Give the extent of all Plasmodium ovale-infected red blood cells.
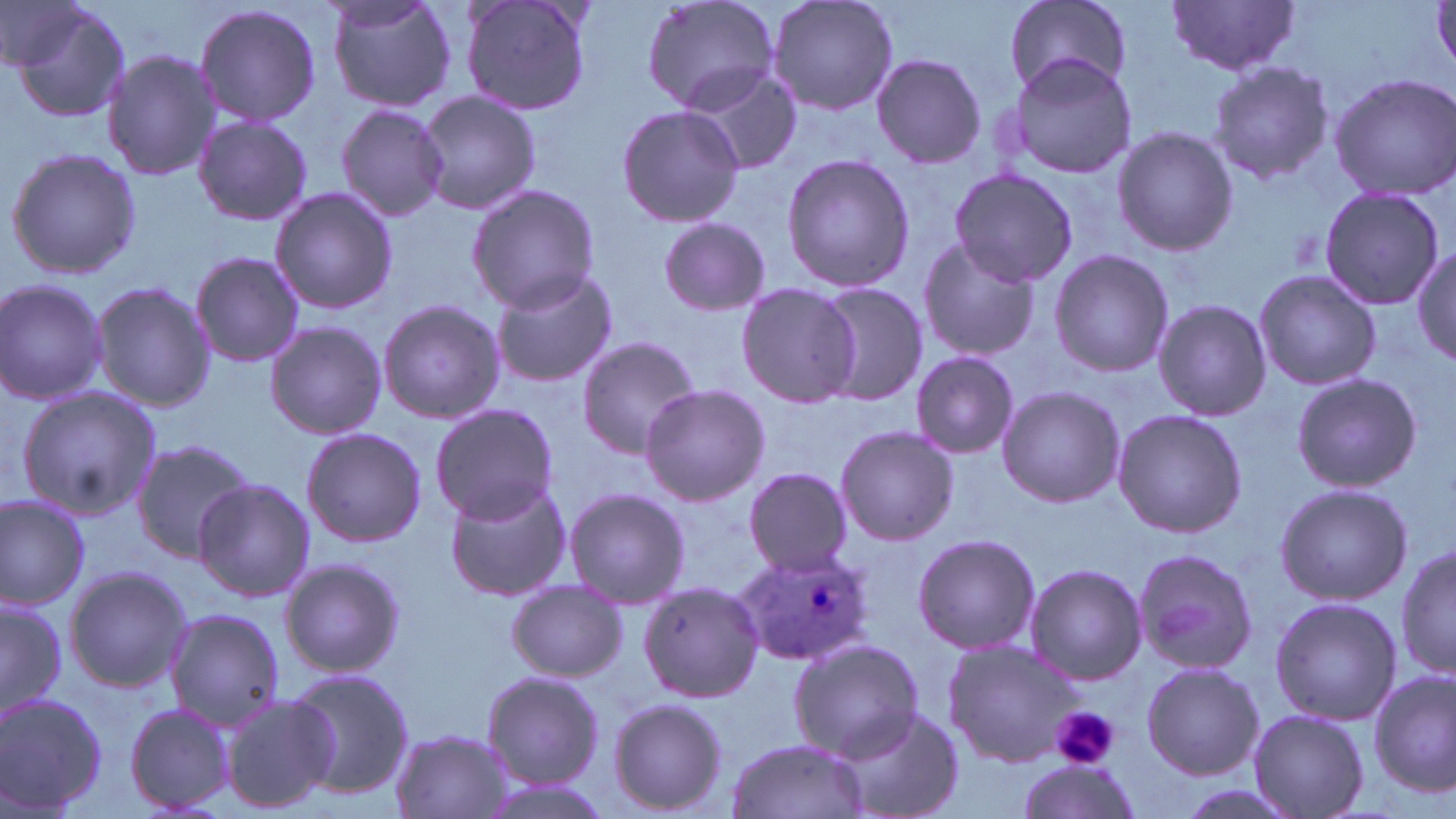

Approximate bounding boxes as [x1, y1, x2, y2] in pixels.
Plasmodium ovale-infected red blood cells: [732, 547, 876, 667].

Summary:
  - Uninfected red blood cell locations: [1, 0, 87, 75], [323, 0, 458, 113], [461, 0, 592, 117], [641, 0, 782, 114], [764, 0, 900, 117], [1003, 1, 1130, 95], [4, 2, 132, 123], [1166, 2, 1303, 78], [193, 3, 323, 129], [103, 51, 222, 180], [1004, 52, 1137, 182], [870, 53, 987, 169], [1207, 60, 1335, 183], [685, 65, 801, 175], [1326, 72, 1456, 203], [415, 90, 542, 214], [336, 103, 448, 223], [616, 103, 745, 229], [192, 115, 313, 226], [1111, 126, 1238, 255], [6, 147, 142, 281], [780, 153, 916, 292], [948, 170, 1080, 286], [465, 183, 600, 313], [1316, 185, 1445, 310], [268, 186, 399, 316], [655, 216, 774, 315], [915, 237, 1042, 360], [1413, 245, 1455, 366], [1049, 248, 1173, 378], [190, 251, 304, 368], [488, 268, 621, 389], [1253, 270, 1382, 390], [0, 278, 109, 406], [735, 280, 861, 408], [88, 281, 216, 412], [814, 281, 928, 406], [377, 299, 505, 425], [1153, 299, 1272, 422], [265, 321, 388, 440], [575, 335, 700, 459], [910, 352, 1019, 457], [1290, 372, 1422, 493], [16, 385, 160, 523], [640, 385, 770, 503], [996, 387, 1126, 508], [430, 403, 557, 524], [1112, 408, 1246, 537], [834, 425, 958, 545], [301, 426, 427, 546], [130, 438, 260, 565], [742, 467, 855, 576], [193, 478, 316, 602], [443, 478, 571, 602], [1272, 482, 1412, 606], [562, 486, 690, 608], [0, 494, 90, 609], [911, 532, 1041, 654], [1395, 543, 1454, 685], [1131, 546, 1258, 677], [280, 557, 405, 678], [1024, 563, 1147, 684], [64, 564, 192, 693], [505, 581, 626, 681], [639, 581, 765, 702], [0, 597, 67, 718], [1269, 597, 1400, 724], [164, 608, 285, 728], [789, 636, 922, 761], [942, 636, 1083, 767], [1142, 661, 1263, 780], [286, 668, 413, 798], [479, 670, 604, 788], [1368, 670, 1455, 793], [0, 693, 107, 817], [218, 693, 339, 814], [607, 697, 730, 814], [125, 703, 237, 814], [835, 703, 962, 819], [1247, 709, 1368, 819], [388, 729, 520, 819], [723, 737, 871, 819], [1016, 758, 1142, 817], [1173, 782, 1302, 819]
  - Platelet locations: [1050, 704, 1119, 770]
  - Slide-level diagnosis: Plasmodium ovale
  - Modality: optical microscopy
  - Image size: 1456×819 pixels
  - Field of view: single
  - Magnification: 1000x
  - Preparation: thin blood film
  - Stain: May-Grünwald-Giemsa